Assess the morphology of the red blood cells.
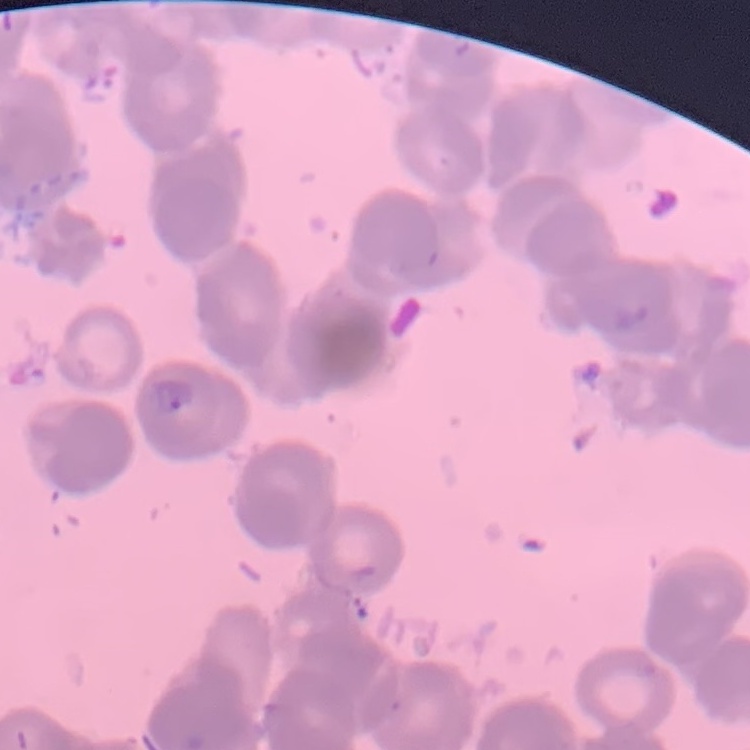
Rouleaux formation.

Square crop of a larger photomicrograph. Thin blood film. Field's or Giemsa stain.